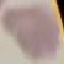

malaria status = uninfected
preparation = thin blood smear
image type = cell patch, automatically extracted from a larger field of view and resized to 64 × 64 pixels
capture = smartphone through the microscope eyepiece
stain = Giemsa